Outline each blood parasite and name the species.
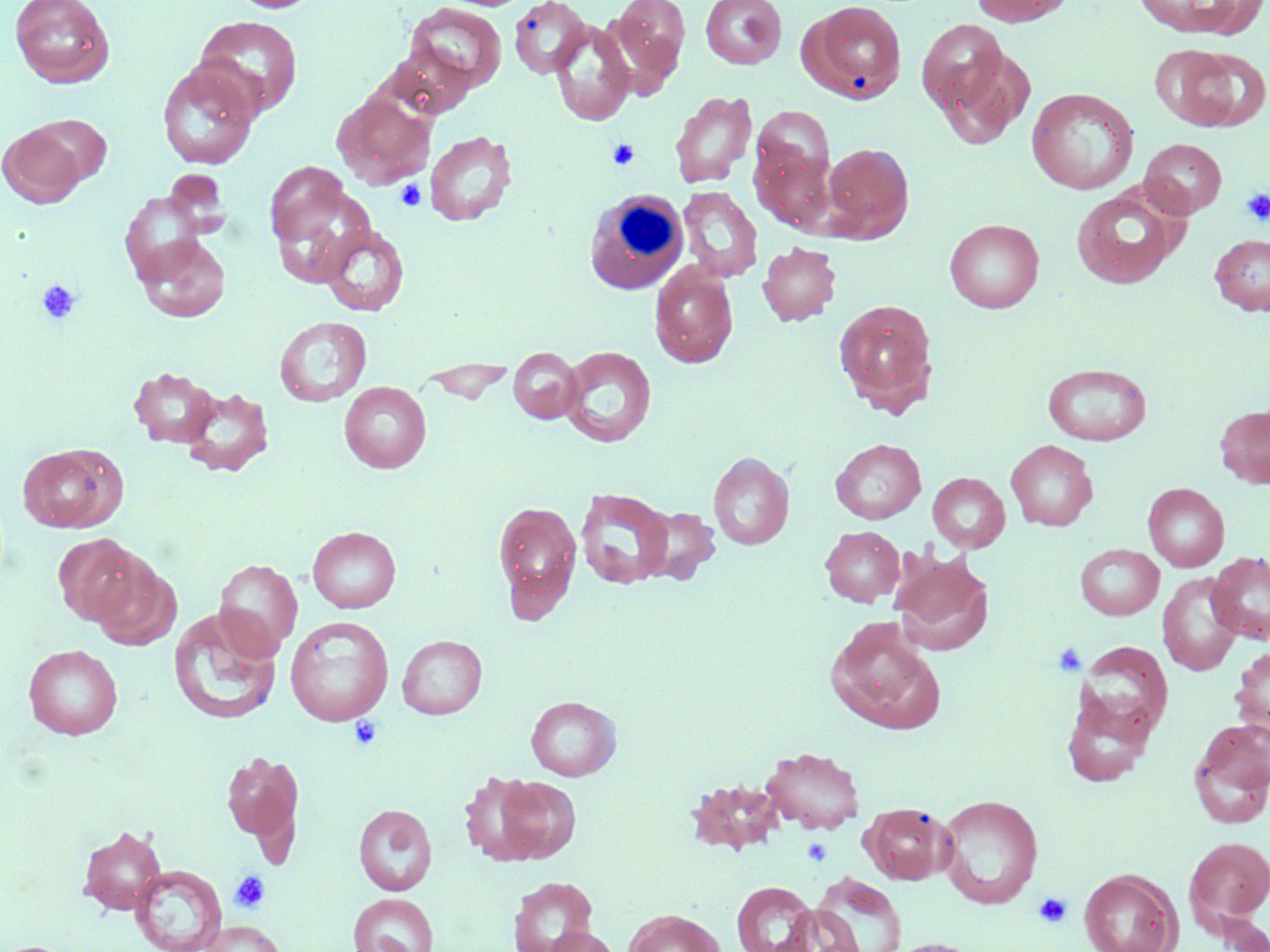

No blood parasites seen.

Summary:
  - Coordinate format: approximate bounding boxes as [x1, y1, x2, y2] in pixels
  - Platelet locations: [608, 139, 640, 169], [394, 180, 426, 211], [1240, 188, 1270, 226], [37, 279, 81, 324], [1052, 642, 1088, 677], [349, 715, 383, 751], [801, 837, 834, 867], [230, 870, 271, 913], [1033, 892, 1073, 929]
  - White blood cell locations: [583, 186, 696, 298]
  - Uninfected red blood cell locations: [10, 0, 115, 88], [228, 0, 322, 13], [606, 0, 691, 92], [700, 0, 787, 69], [967, 0, 1074, 26], [509, 1, 592, 79], [800, 1, 908, 104], [1132, 1, 1263, 38], [405, 2, 508, 93], [193, 15, 304, 117], [549, 20, 636, 127], [919, 27, 1032, 147], [380, 43, 477, 119], [1148, 44, 1239, 129], [1182, 46, 1270, 130], [156, 61, 260, 169], [1026, 87, 1139, 194], [331, 90, 436, 188], [670, 91, 758, 189], [749, 110, 838, 231], [28, 114, 112, 186], [1, 123, 87, 208], [425, 130, 518, 227], [1140, 138, 1226, 218], [822, 142, 914, 242], [264, 161, 365, 278], [164, 169, 230, 239], [678, 186, 763, 282], [1071, 187, 1182, 290], [120, 190, 208, 283], [945, 218, 1044, 313], [319, 224, 410, 316], [1209, 233, 1270, 316], [135, 235, 230, 322], [758, 242, 841, 327], [649, 262, 739, 368], [833, 298, 939, 413], [274, 316, 371, 407], [558, 345, 657, 448], [508, 347, 583, 424], [418, 359, 516, 404], [1042, 362, 1152, 446], [129, 366, 221, 448], [339, 381, 431, 473], [181, 387, 273, 477], [1214, 403, 1270, 490], [831, 438, 925, 524], [1006, 439, 1098, 531], [17, 444, 126, 533], [708, 452, 794, 550], [928, 472, 1010, 553], [1142, 482, 1229, 572], [576, 488, 674, 590], [492, 498, 583, 623], [639, 506, 720, 584], [307, 526, 401, 613], [820, 526, 905, 606], [53, 533, 146, 626], [1075, 543, 1164, 620], [1208, 551, 1270, 644], [890, 552, 994, 656], [89, 555, 180, 651], [214, 559, 303, 656], [1157, 573, 1243, 675], [168, 607, 283, 725], [285, 615, 394, 725], [825, 616, 946, 734], [397, 635, 487, 719], [1077, 641, 1173, 737], [1230, 643, 1270, 740], [23, 644, 123, 739], [1061, 688, 1155, 788], [525, 696, 621, 781], [1188, 718, 1270, 828], [762, 746, 865, 833], [222, 749, 304, 851], [473, 771, 582, 865], [936, 793, 1043, 909], [861, 802, 953, 885], [353, 804, 437, 896], [78, 825, 167, 914], [1183, 836, 1270, 931], [130, 865, 227, 952], [1078, 868, 1181, 952], [811, 873, 906, 952], [507, 876, 598, 952], [732, 881, 818, 952], [348, 893, 438, 952], [778, 904, 865, 952], [623, 908, 725, 952], [1208, 912, 1270, 951], [196, 919, 287, 952], [542, 926, 622, 952], [877, 937, 990, 952]
  - Slide-level diagnosis: negative for blood parasites
  - Stain: May-Grünwald-Giemsa
  - Field of view: one of a larger specimen
  - Preparation: thin blood smear
  - Magnification: 1000x
  - Modality: optical microscopy
  - Image size: 1270×952 pixels